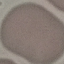
Summary:
  - Malaria status: uninfected
  - Image type: cell patch, automatically extracted from a larger field of view and resized to 64 × 64 pixels
  - Stain: Giemsa
  - Preparation: thin blood film
  - Capture: smartphone through the microscope eyepiece